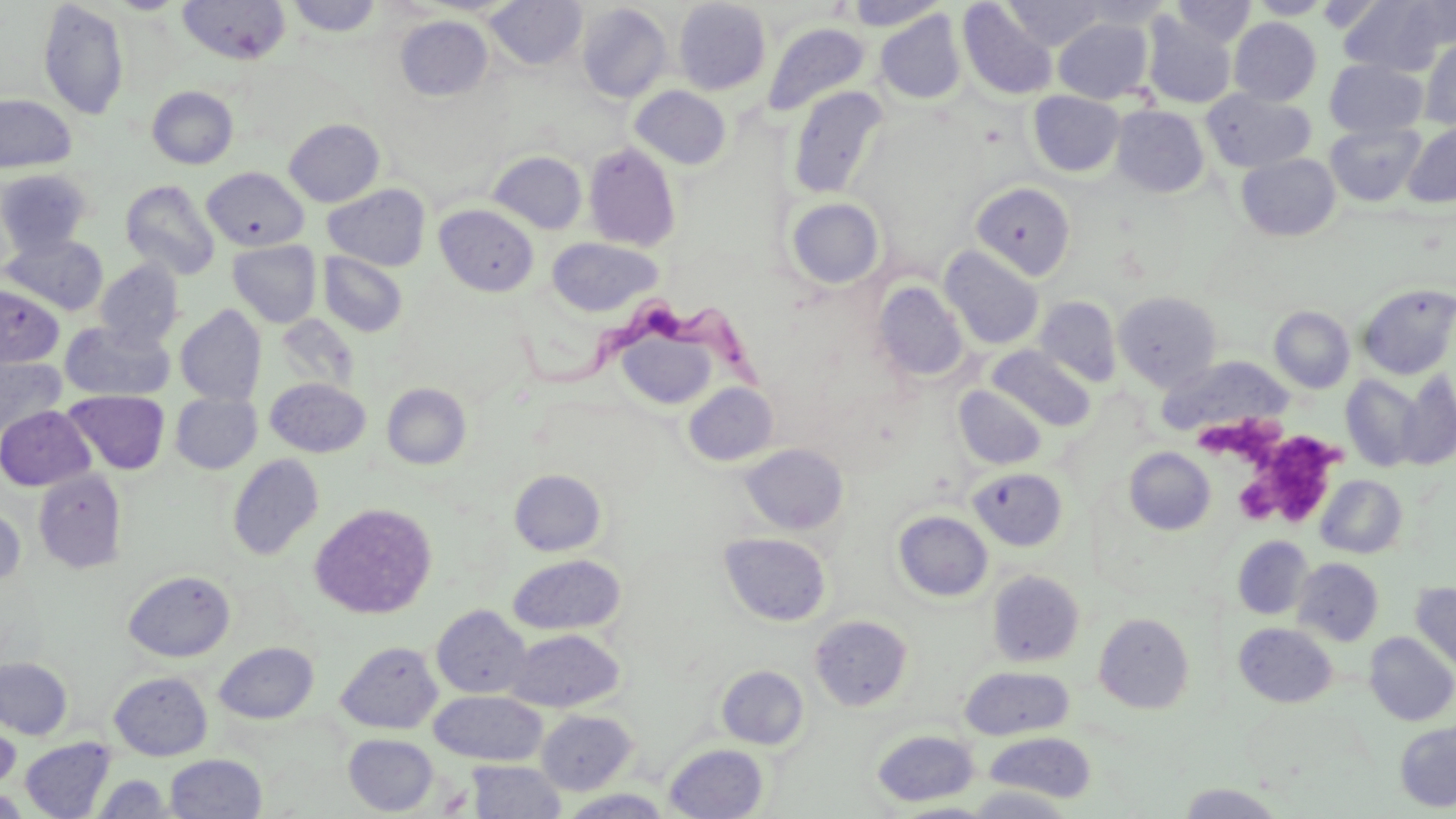

Summary:
  - Coordinate format: approximate bounding boxes as (x1,y1)-(x2,y2) corner pairs in pixels
  - Trypanosoma brucei locations: (516,303)-(775,397)
  - Uninfected red blood cell locations: (178,0)-(291,66), (287,0)-(383,37), (485,0)-(587,70), (673,0)-(771,95), (1004,0)-(1105,49), (1076,0)-(1174,28), (1249,0)-(1331,19), (1340,0)-(1455,76), (38,1)-(128,120), (844,1)-(948,30), (957,1)-(1057,100), (1170,1)-(1257,46), (576,3)-(672,103), (673,9)-(871,100), (876,11)-(965,104), (1143,14)-(1236,109), (395,16)-(493,100), (1053,18)-(1153,104), (1229,18)-(1321,105), (762,23)-(871,117), (1420,35)-(1456,131), (1325,59)-(1428,138), (630,85)-(731,169), (147,86)-(238,169), (788,86)-(888,199), (1202,89)-(1315,173), (1028,91)-(1124,177), (0,95)-(76,172), (1111,106)-(1209,197), (284,118)-(384,207), (1325,122)-(1425,206), (1403,122)-(1456,207), (583,143)-(681,251), (489,151)-(587,234), (1236,154)-(1341,242), (201,167)-(309,251), (1,168)-(94,257), (120,179)-(221,281), (971,182)-(1076,281), (322,183)-(431,271), (786,198)-(884,289), (435,205)-(538,296), (2,233)-(109,316), (547,237)-(662,316), (228,241)-(322,327), (939,245)-(1044,350), (318,252)-(408,337), (96,260)-(184,350), (873,281)-(967,383), (0,283)-(64,368), (1357,283)-(1456,379), (1114,291)-(1222,390), (1035,296)-(1122,387), (175,305)-(267,406), (1270,306)-(1355,394), (59,321)-(175,402), (622,337)-(724,408), (987,346)-(1095,431), (1154,355)-(1293,437), (0,357)-(66,442), (1341,373)-(1425,472), (1395,373)-(1456,470), (265,378)-(370,457), (684,382)-(779,466), (382,383)-(471,469), (954,385)-(1048,470), (63,390)-(169,474), (171,394)-(261,474), (0,405)-(95,490), (740,443)-(848,535), (1124,447)-(1215,535), (227,454)-(324,560), (967,467)-(1068,551), (33,469)-(127,574), (509,469)-(606,556), (1316,475)-(1407,558), (310,502)-(437,619), (0,504)-(26,591), (893,510)-(993,602), (719,532)-(832,626), (1232,536)-(1313,619), (508,554)-(626,635), (1293,557)-(1384,646), (123,570)-(236,662), (986,570)-(1084,666), (1410,583)-(1456,677), (432,605)-(531,698), (1094,613)-(1194,713), (810,615)-(912,711), (1234,623)-(1337,707), (504,628)-(625,712), (1364,632)-(1456,725), (336,641)-(442,733), (214,642)-(318,724), (0,657)-(72,739), (716,665)-(809,750), (960,666)-(1075,740), (109,671)-(212,760), (430,690)-(546,765), (537,709)-(637,795), (0,717)-(20,795), (1395,721)-(1456,812), (870,729)-(980,807), (984,732)-(1096,803), (344,734)-(439,815), (19,738)-(116,817), (664,744)-(768,819), (164,753)-(266,818), (466,761)-(567,818), (92,773)-(173,817), (1178,783)-(1287,818), (962,786)-(1078,818), (0,789)-(31,818), (560,789)-(674,818)
  - Platelet locations: (1204,417)-(1280,469), (1270,435)-(1341,483), (1235,478)-(1276,525), (1272,480)-(1331,528)
  - Slide-level diagnosis: Trypanosoma brucei
  - Modality: light microscopy
  - Image size: 1456×819 pixels
  - Preparation: thin blood smear
  - Magnification: 1000x
  - Stain: May-Grünwald-Giemsa
  - Field of view: single